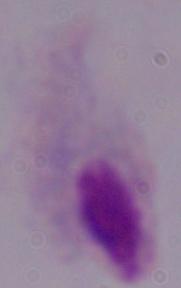
Micrograph. Captured at 1000x magnification. A trichomonad is shown.